Classify this cell by malaria status.
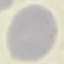

Uninfected.

preparation: thin smear
capture: smartphone through the microscope eyepiece
image_type: automatically extracted cell patch, resized to 64 × 64 pixels
stain: Giemsa